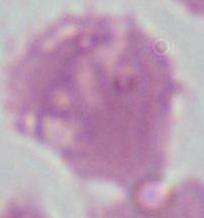

Micrograph. An erythrocyte is seen. Captured at 1000x magnification.